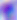
{
  "identification": "Toxoplasma gondii",
  "magnification": "400x",
  "modality": "micrograph"
}